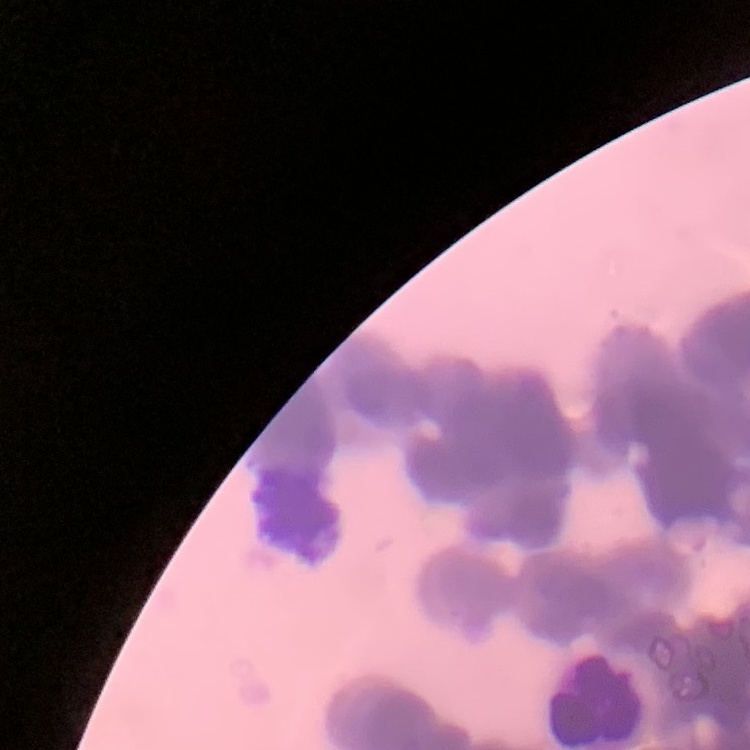

red blood cell morphology = rouleaux formation
preparation = thin blood film
stain = Field's or Giemsa
image type = square crop of a larger photomicrograph